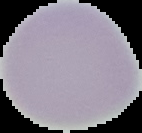
Image is 142×133 pixels. Result: negative for malaria parasites. From a thin blood film. The area outside the segmented cell region is set to black.